Evaluate for Plasmodium parasites.
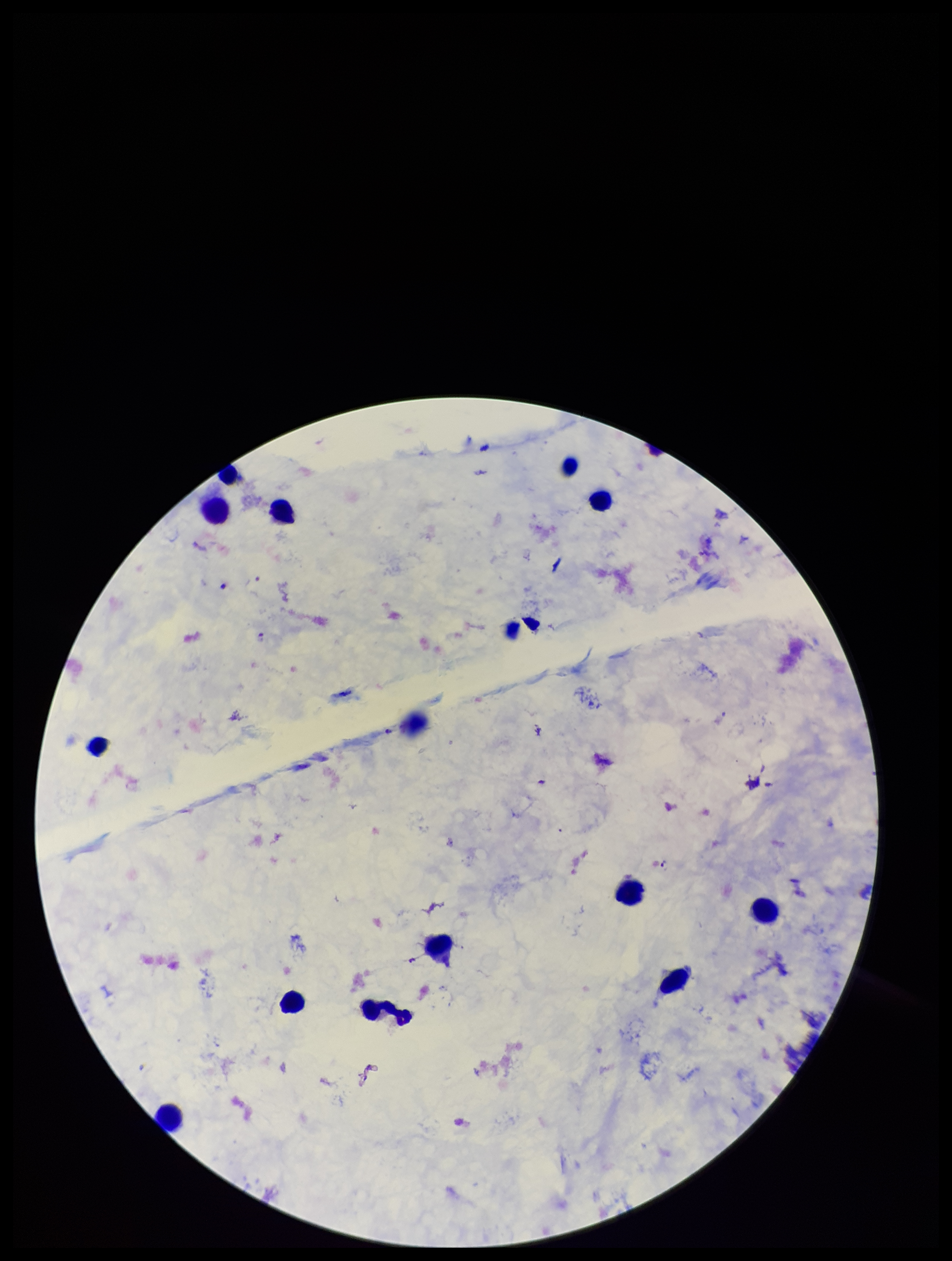
Detected.

Stained with Giemsa. Parasite count: 1. Patient malaria status: positive. Preparation: thick. Single field of view. Image is 952×1261 pixels. Species reported for this patient: Plasmodium falciparum. Photographed through the microscope eyepiece with a smartphone camera. Leukocyte count: 12.